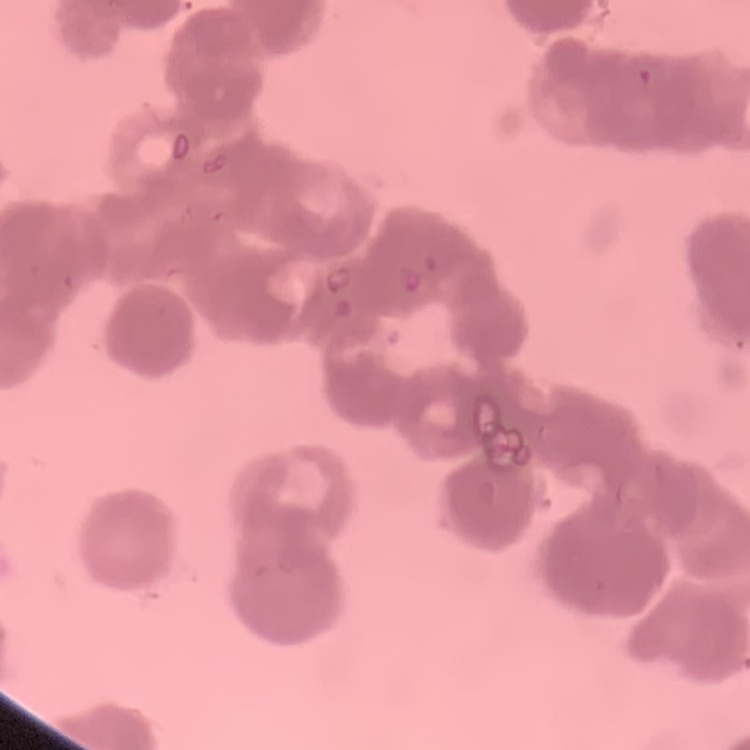
Summary:
  - Red blood cell morphology: rouleaux formation
  - Preparation: thin blood smear
  - Stain: Field's or Giemsa
  - Image type: one tile cut from a larger photomicrograph